Assess this cell for malaria.
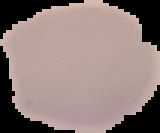
It is uninfected.

The area outside the segmented cell region is set to black. Image is 160×133 pixels. From a thin blood smear.